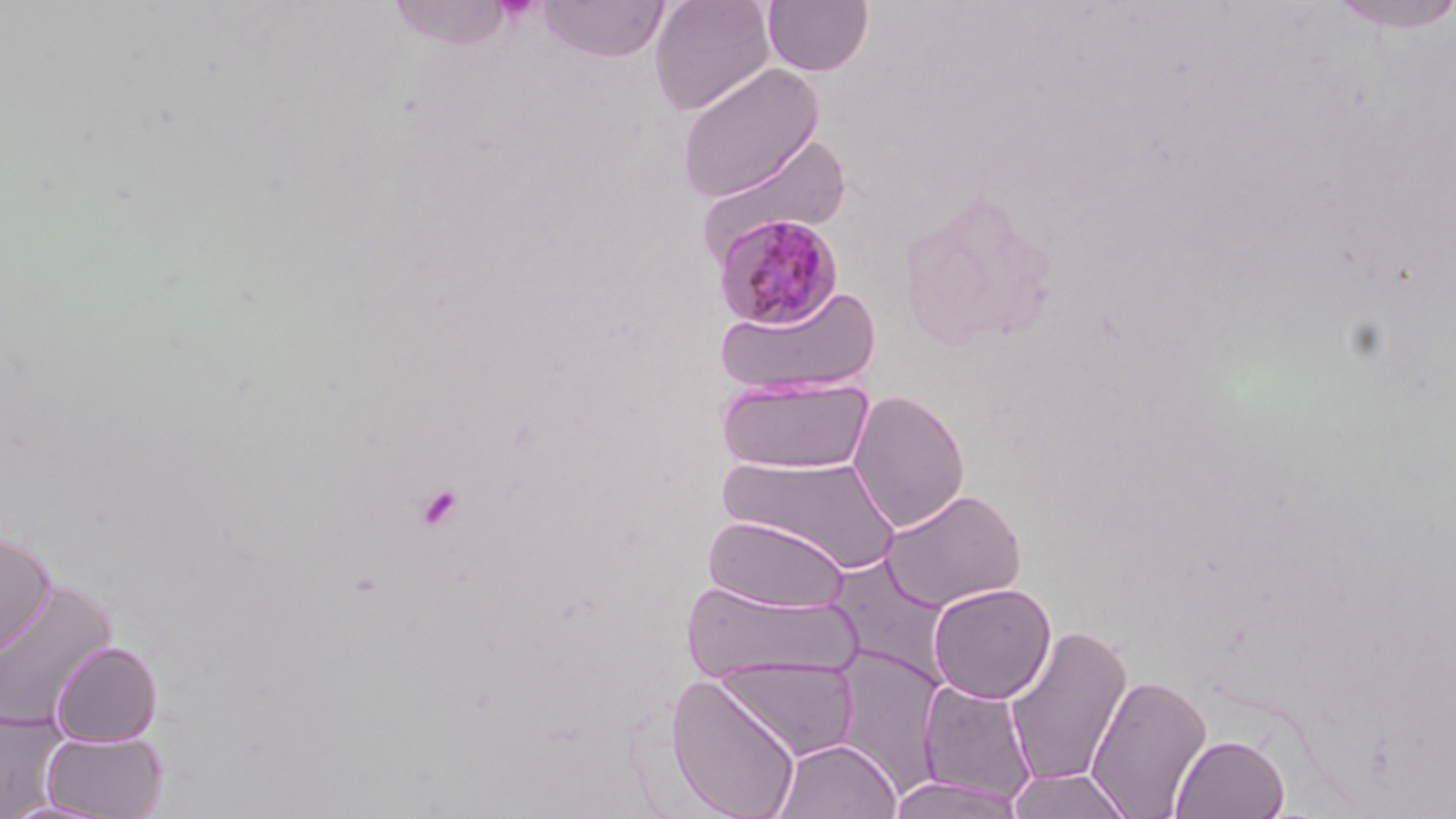

slide_level_diagnosis: Plasmodium malariae
stain: May-Grünwald-Giemsa
modality: optical microscopy
preparation: thin blood smear
field_of_view: one of a larger specimen
uninfected_red_blood_cell_locations: 'approximate bounding boxes as (x1,y1)-(x2,y2) corner pairs in pixels: (387,0)-(519,50), (536,0)-(672,62), (648,0)-(775,116), (763,0)-(874,76), (1324,0)-(1456,34), (675,63)-(825,203), (694,131)-(853,262), (715,285)-(881,396), (717,376)-(874,475), (847,388)-(970,533), (718,454)-(904,576), (880,488)-(1027,611), (703,514)-(850,613), (0,530)-(56,657), (827,555)-(955,684), (0,578)-(118,735), (683,580)-(862,685), (928,583)-(1056,703), (1003,624)-(1134,788), (51,640)-(163,745), (829,645)-(948,793), (713,658)-(860,762), (665,672)-(802,819), (1085,673)-(1212,818), (916,678)-(1039,806), (0,712)-(67,816), (41,731)-(168,818), (1171,733)-(1291,818), (770,737)-(902,819), (1005,767)-(1137,818), (885,775)-(1026,817), (0,797)-(123,818)'
platelet_locations: 'approximate bounding boxes as (x1,y1)-(x2,y2) corner pairs in pixels: (413,481)-(464,532)'
magnification: 1000x
plasmodium_malariae_infected_red_blood_cell_locations: 'approximate bounding boxes as (x1,y1)-(x2,y2) corner pairs in pixels: (713,212)-(846,332)'
image_size: 1456×819 pixels